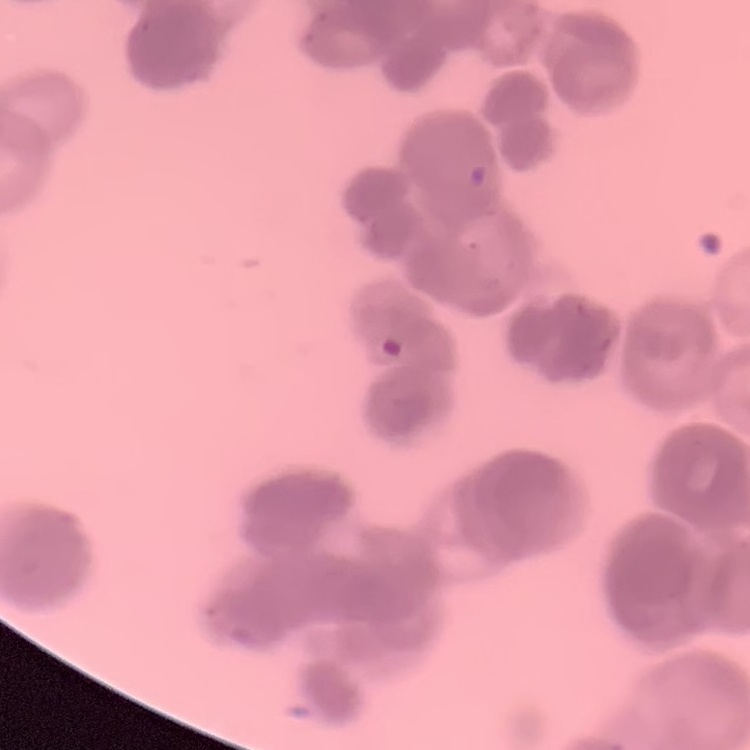

red blood cell morphology = rouleaux formation
preparation = thin blood film
image type = one tile cut from a larger photomicrograph
stain = Field's or Giemsa